Assess this cell for malaria.
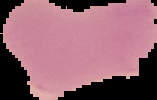
Uninfected.

From a thin blood film. The area outside the segmented cell region is set to black. Image is 157×100 pixels.